Report the malaria status of this cell.
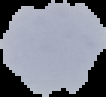
It is uninfected.

image size = 106×97 pixels
image type = segmented cell region with the area outside set to black
preparation = thin blood smear